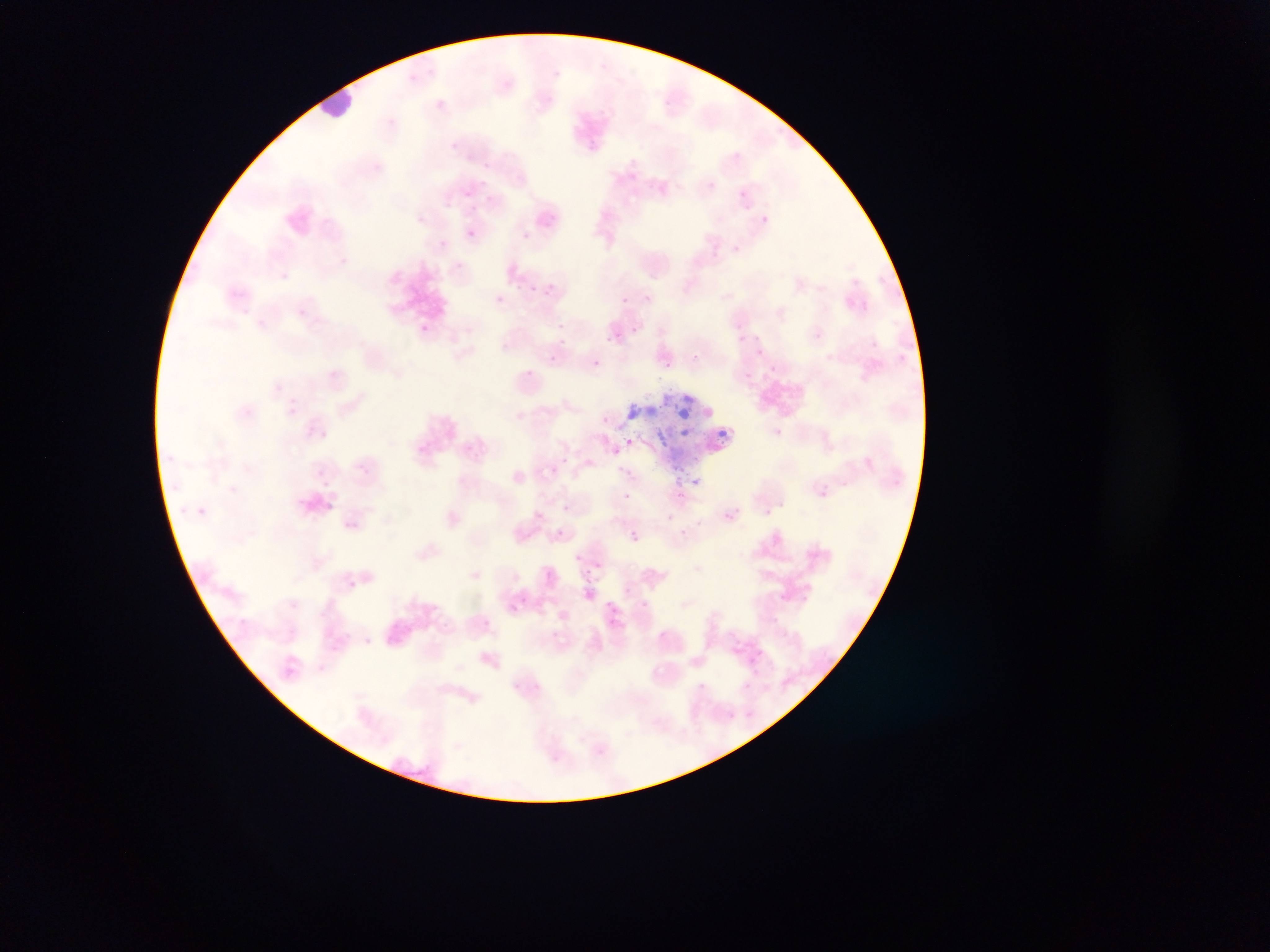
{
  "malaria_parasite_locations": "approximate bounding boxes as [left, top, right, bottom] in pixels: [554, 69, 562, 78], [408, 74, 423, 82], [586, 140, 600, 152], [627, 175, 637, 183], [739, 190, 749, 199], [464, 191, 473, 198], [763, 214, 770, 226], [543, 215, 556, 227], [465, 229, 476, 237], [524, 232, 533, 245], [437, 240, 447, 249], [733, 242, 742, 255], [453, 260, 464, 269], [852, 277, 860, 285], [548, 281, 555, 290], [512, 284, 522, 292], [531, 284, 541, 293], [494, 295, 504, 304], [620, 297, 628, 304], [736, 323, 743, 333], [420, 324, 429, 331], [631, 324, 643, 333], [814, 330, 823, 340], [750, 332, 762, 342], [734, 333, 745, 346], [608, 338, 616, 346], [559, 339, 570, 345], [756, 348, 763, 356], [550, 351, 560, 362], [695, 352, 703, 361], [590, 359, 602, 371], [666, 359, 676, 375], [520, 366, 538, 382], [768, 366, 777, 374], [285, 405, 298, 417], [604, 414, 610, 428], [318, 428, 329, 439], [720, 428, 731, 437], [773, 428, 784, 436], [625, 436, 636, 446], [611, 447, 621, 457], [562, 457, 570, 467], [586, 459, 594, 468], [356, 463, 368, 474], [315, 468, 324, 478], [691, 476, 701, 486], [676, 488, 687, 499], [819, 489, 828, 498], [622, 491, 631, 501], [324, 501, 335, 510], [563, 503, 569, 511], [732, 504, 738, 512], [197, 506, 206, 515], [764, 509, 772, 517], [724, 513, 733, 522], [668, 514, 677, 521], [345, 520, 357, 530], [553, 528, 568, 534], [631, 532, 640, 542], [573, 552, 583, 561], [598, 561, 606, 567], [545, 569, 555, 579], [584, 578, 597, 586], [623, 585, 632, 594], [782, 592, 788, 601], [800, 592, 809, 607], [520, 596, 529, 606], [640, 599, 648, 608], [607, 600, 616, 607], [508, 602, 520, 612], [770, 616, 778, 623], [482, 617, 491, 631], [608, 619, 616, 629], [554, 630, 562, 639], [757, 649, 767, 656], [746, 655, 754, 666], [698, 682, 706, 690], [743, 682, 752, 691] | approximate [x, y] pixel centers of objects too small to bound: [438, 104], [454, 145], [487, 165], [482, 184], [489, 199], [473, 206], [619, 333], [589, 571]",
  "preparation": "thin blood smear",
  "country": "Ghana",
  "field_of_view": "single",
  "leukocyte_locations": "approximate bounding boxes as [left, top, right, bottom] in pixels: [317, 76, 360, 126]",
  "image_size": "1270×952 pixels",
  "capture": "mobile-phone photograph through a microscope"
}